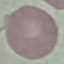
result = negative for malaria parasites
preparation = thin smear
stain = Giemsa
image type = automatically extracted cell patch, resized to 64 × 64 pixels
capture = smartphone through the microscope eyepiece